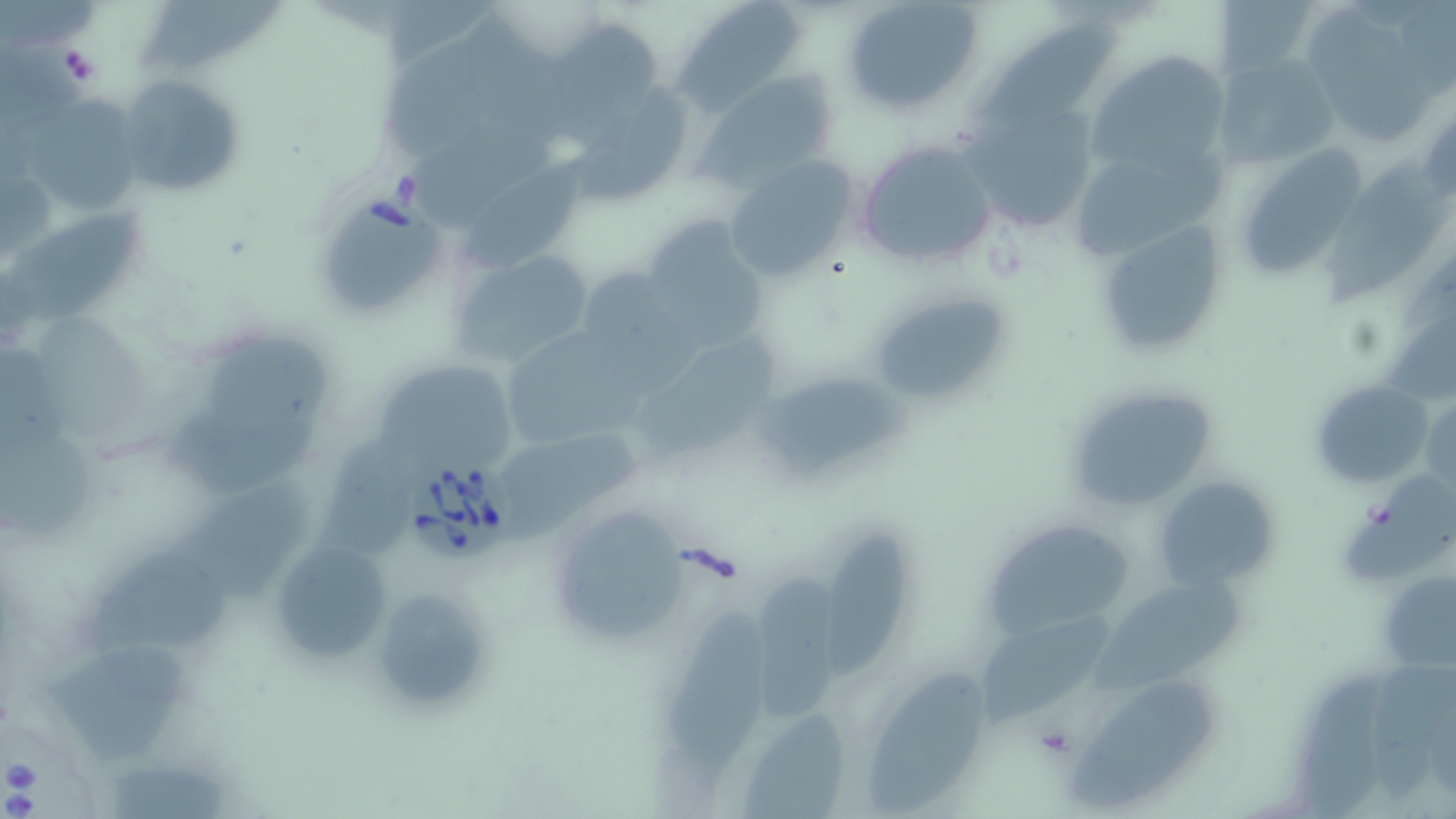

Summary:
  - Coordinate format: approximate bounding boxes as (x1, y1, x2, y2) in pixels
  - Uninfected red blood cell locations: (840, 0, 985, 116), (1211, 0, 1324, 82), (674, 1, 807, 113), (133, 2, 283, 68), (1311, 12, 1430, 139), (386, 19, 546, 152), (983, 19, 1137, 130), (543, 23, 666, 150), (1084, 52, 1234, 188), (1211, 53, 1342, 170), (693, 70, 842, 191), (114, 73, 244, 198), (579, 83, 692, 205), (23, 90, 141, 209), (958, 96, 1102, 231), (415, 110, 558, 231), (853, 137, 1001, 273), (1231, 141, 1369, 283), (464, 147, 601, 275), (721, 157, 857, 284), (1317, 158, 1453, 304), (1, 208, 145, 330), (1090, 217, 1228, 359), (640, 220, 766, 355), (452, 249, 598, 372), (573, 266, 681, 366), (864, 287, 1012, 410), (505, 328, 656, 444), (637, 335, 783, 462), (200, 336, 347, 432), (377, 365, 523, 465), (763, 377, 908, 472), (1308, 378, 1433, 489), (1065, 386, 1217, 512), (172, 403, 324, 493), (505, 429, 642, 551), (0, 430, 103, 539), (1342, 470, 1456, 586), (1155, 473, 1280, 591), (166, 479, 320, 611), (543, 496, 695, 652), (988, 525, 1140, 639), (824, 531, 912, 684), (269, 538, 394, 664), (67, 548, 239, 660), (753, 572, 839, 727), (1381, 575, 1456, 674), (1094, 579, 1248, 693), (374, 595, 495, 706), (666, 601, 787, 787), (988, 615, 1119, 729), (44, 645, 194, 761), (1290, 661, 1413, 819), (865, 668, 997, 819), (1071, 681, 1221, 807), (740, 706, 854, 818), (103, 764, 232, 819)
  - Platelet locations: (1032, 723, 1078, 759)
  - Babesia divergens-infected red blood cell locations: (310, 193, 454, 319), (405, 455, 519, 567), (0, 712, 100, 819)
  - Slide-level diagnosis: Babesia divergens
  - Preparation: thin blood film
  - Field of view: single
  - Image size: 1456×819 pixels
  - Stain: May-Grünwald-Giemsa
  - Magnification: 1000x
  - Modality: light microscopy